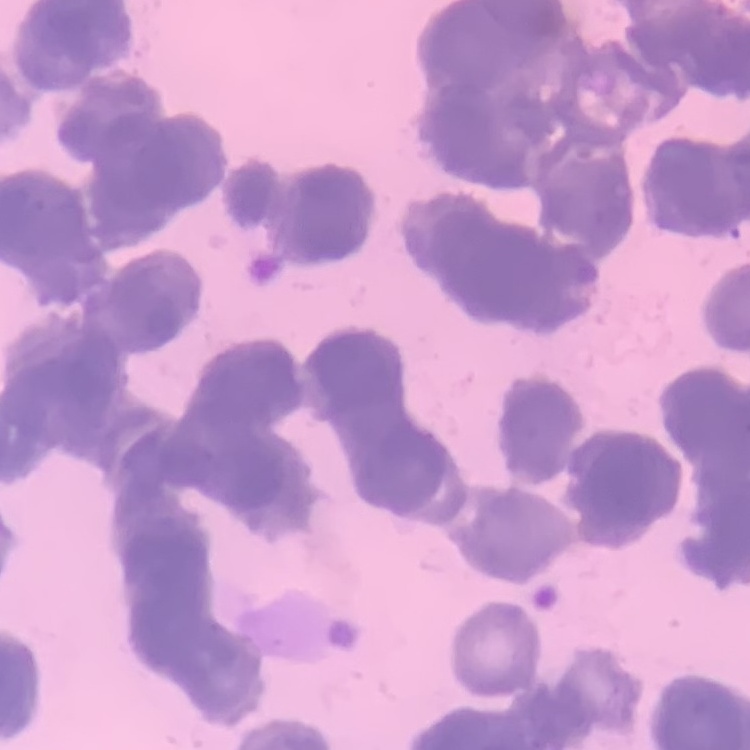
Summary:
  - Red blood cell morphology: rouleaux formation
  - Stain: Field's or Giemsa
  - Image type: one tile cut from a larger photomicrograph
  - Preparation: thin blood smear